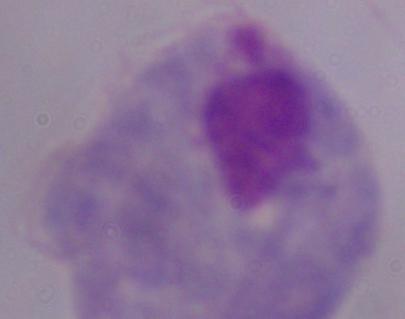

Photomicrograph. Captured at 1000x magnification. A trichomonad is shown.